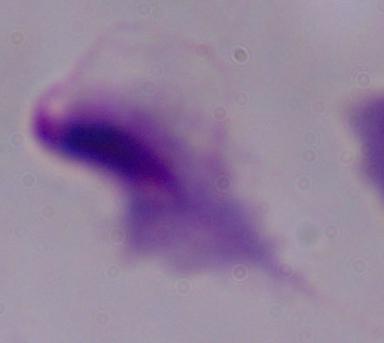
Micrograph. 1000x magnification. A trichomonad is seen.